Locate cells.
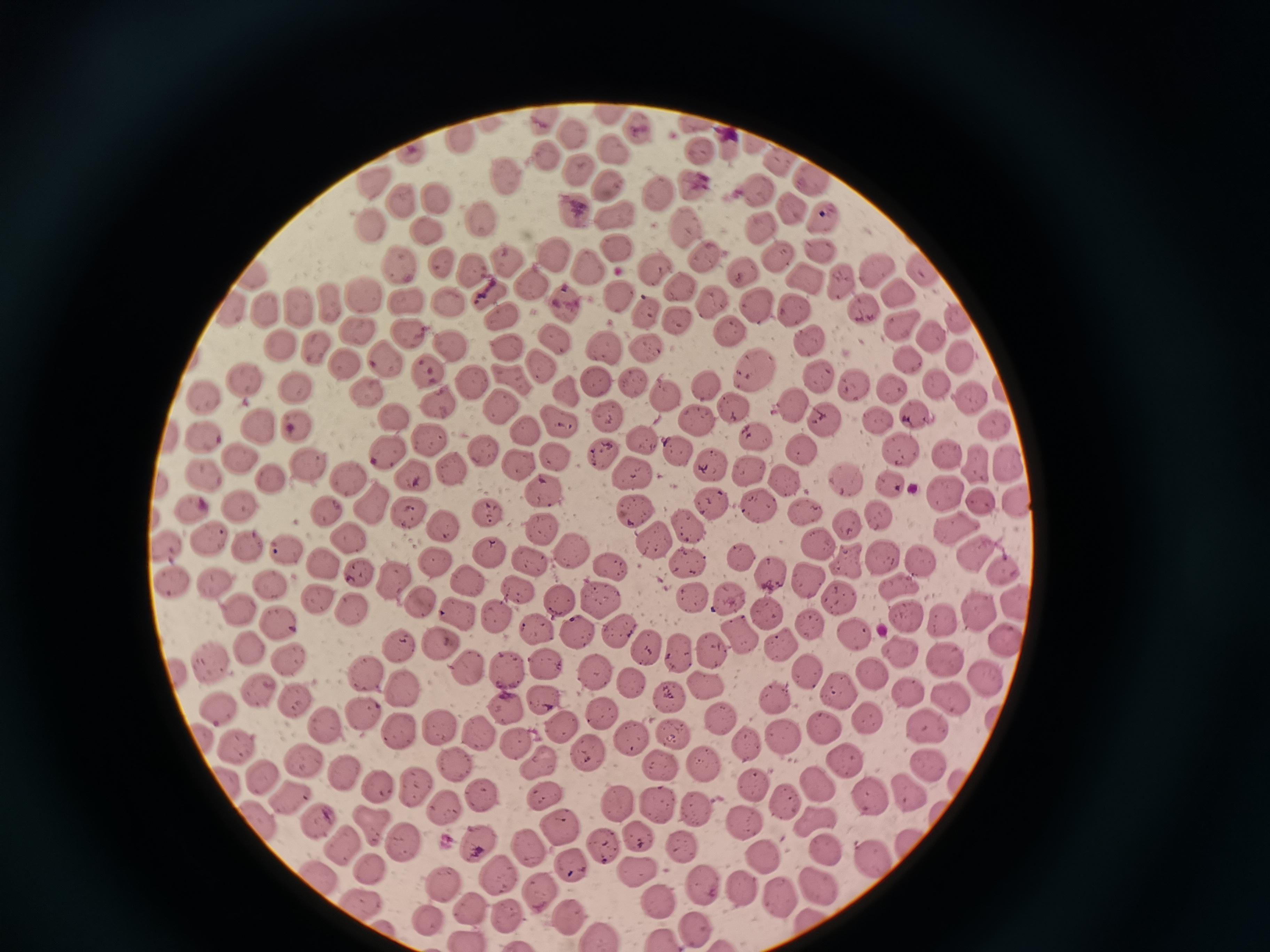
Approximate centers as {x, y} in pixels.
Cells: {606, 111}, {545, 119}, {637, 126}, {695, 126}, {568, 135}, {726, 140}, {749, 141}, {461, 142}, {608, 144}, {701, 151}, {411, 153}, {548, 157}, {777, 161}, {577, 171}, {508, 178}, {816, 178}, {379, 179}, {694, 182}, {608, 185}, {760, 189}, {659, 190}, {408, 196}, {435, 199}, {791, 210}, {574, 212}, {614, 213}, {828, 218}, {369, 220}, {760, 223}, {687, 224}, {484, 225}, {430, 230}, {616, 251}, {776, 252}, {818, 252}, {557, 253}, {701, 255}, {507, 260}, {402, 264}, {475, 264}, {443, 265}, {590, 266}, {654, 270}, {873, 270}, {919, 270}, {745, 274}, {808, 275}, {255, 277}, {842, 281}, {530, 285}, {678, 288}, {493, 292}, {901, 292}, {364, 297}, {618, 298}, {450, 302}, {714, 303}, {563, 305}, {231, 306}, {329, 306}, {407, 306}, {759, 306}, {299, 307}, {794, 308}, {268, 309}, {866, 310}, {647, 312}, {501, 317}, {957, 319}, {679, 320}, {901, 326}, {358, 327}, {730, 331}, {408, 332}, {931, 337}, {556, 339}, {813, 339}, {281, 344}, {318, 344}, {449, 345}, {605, 345}, {647, 348}, {507, 350}, {906, 357}, {960, 357}, {385, 359}, {345, 361}, {540, 363}, {431, 368}, {755, 369}, {816, 373}, {510, 377}, {595, 378}, {245, 379}, {469, 379}, {294, 382}, {936, 382}, {632, 383}, {705, 384}, {852, 385}, {1000, 386}, {364, 387}, {892, 387}, {205, 392}, {566, 392}, {664, 395}, {970, 395}, {441, 402}, {498, 403}, {792, 404}, {737, 411}, {916, 411}, {606, 414}, {392, 416}, {874, 418}, {696, 420}, {560, 421}, {826, 422}, {295, 423}, {993, 423}, {257, 426}, {527, 430}, {202, 434}, {428, 436}, {640, 437}, {758, 438}, {900, 449}, {385, 450}, {802, 450}, {482, 451}, {946, 453}, {678, 454}, {603, 455}, {556, 456}, {237, 457}, {310, 463}, {975, 464}, {1005, 464}, {517, 465}, {449, 466}, {750, 467}, {716, 468}, {411, 472}, {632, 472}, {202, 473}, {268, 476}, {846, 477}, {349, 480}, {786, 483}, {891, 484}, {544, 489}, {942, 491}, {1020, 498}, {708, 502}, {981, 502}, {239, 503}, {376, 503}, {759, 505}, {191, 507}, {328, 508}, {632, 511}, {407, 512}, {804, 513}, {878, 513}, {483, 514}, {846, 521}, {446, 524}, {688, 525}, {954, 527}, {541, 528}, {349, 534}, {211, 536}, {246, 542}, {166, 544}, {656, 545}, {286, 549}, {815, 549}, {489, 552}, {973, 553}, {570, 554}, {738, 556}, {882, 558}, {844, 559}, {320, 562}, {432, 562}, {528, 562}, {917, 564}, {691, 565}, {611, 567}, {1002, 567}, {359, 572}, {765, 572}, {172, 574}, {804, 576}, {267, 579}, {470, 579}, {397, 580}, {897, 586}, {217, 587}, {518, 592}, {595, 596}, {838, 596}, {318, 599}, {561, 599}, {692, 599}, {1015, 602}, {417, 603}, {728, 604}, {977, 608}, {351, 610}, {245, 612}, {457, 613}, {770, 613}, {906, 616}, {497, 618}, {942, 618}, {811, 622}, {280, 625}, {535, 630}, {615, 631}, {579, 633}, {855, 634}, {740, 635}, {1003, 637}, {780, 640}, {439, 643}, {400, 645}, {247, 648}, {647, 648}, {680, 648}, {711, 651}, {901, 655}, {946, 656}, {289, 657}, {545, 663}, {504, 665}, {208, 666}, {467, 666}, {176, 671}, {371, 671}, {811, 671}, {594, 672}, {871, 672}, {628, 679}, {708, 680}, {984, 682}, {402, 689}, {262, 690}, {837, 691}, {909, 691}, {669, 696}, {947, 698}, {545, 699}, {776, 699}, {297, 701}, {219, 707}, {507, 707}, {364, 713}, {605, 715}, {719, 717}, {995, 718}, {860, 719}, {563, 725}, {924, 725}, {441, 726}, {327, 728}, {399, 731}, {825, 731}, {678, 732}, {482, 734}, {631, 735}, {784, 736}, {205, 737}, {516, 740}, {234, 742}, {747, 743}, {590, 754}, {309, 762}, {703, 762}, {539, 763}, {665, 763}, {846, 763}, {930, 763}, {453, 764}, {258, 771}, {346, 772}, {225, 780}, {817, 780}, {956, 782}, {753, 786}, {384, 787}, {414, 788}, {911, 790}, {481, 791}, {288, 795}, {543, 795}, {782, 800}, {875, 801}, {654, 802}, {621, 804}, {443, 809}, {695, 810}, {939, 813}, {747, 819}, {817, 820}, {259, 821}, {321, 823}, {559, 825}, {373, 826}, {635, 837}, {479, 840}, {341, 845}, {404, 845}, {602, 845}, {908, 847}, {529, 848}, {825, 848}, {682, 850}, {766, 857}, {869, 857}, {569, 863}, {636, 868}, {369, 869}, {496, 872}, {318, 877}, {445, 882}, {702, 886}, {743, 886}, {822, 888}, {540, 889}, {362, 900}, {778, 901}, {659, 902}, {470, 911}, {567, 915}, {507, 917}, {431, 919}, {693, 926}, {599, 934}, {468, 937}, {662, 937}.

Summary:
  - Stain: Giemsa
  - Image size: 1270×952 pixels
  - Preparation: thin blood film
  - Capture: smartphone camera at the microscope eyepiece
  - Field of view: single